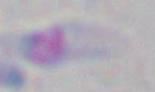

Captured at 1000x magnification. Toxoplasma gondii is shown. Micrograph.